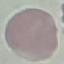 Malaria status: uninfected. Photographed with a smartphone camera at the microscope eyepiece. Cell patch, automatically extracted from a larger field of view and resized to 64 × 64 pixels. Giemsa-stained preparation. Thin smear of blood.